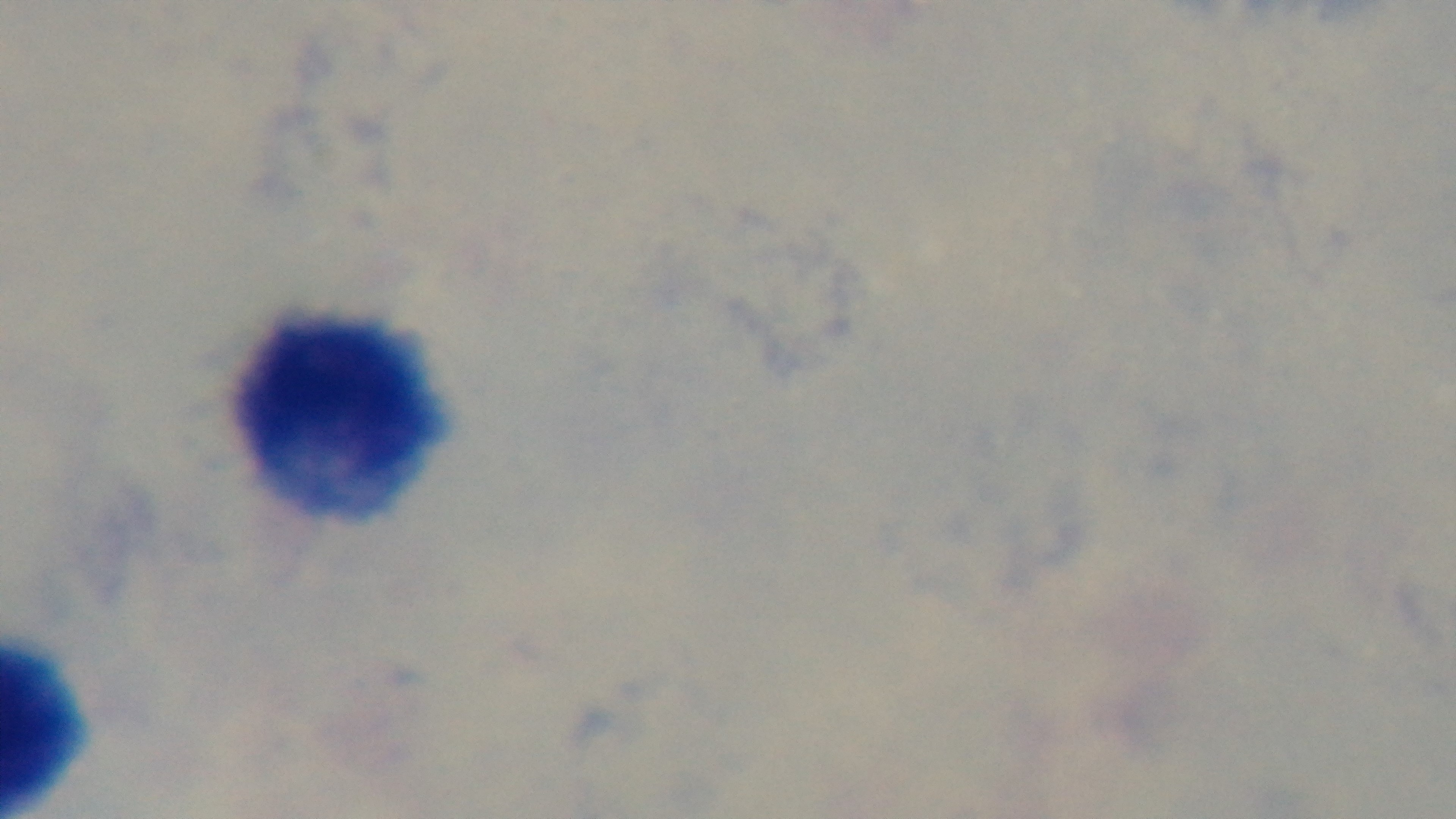
Preparation: thick blood film. Giemsa-stained. Mounted 4K digital camera. 100x oil-immersion objective. Single field of view. Light microscopy. Malaria status: uninfected.